Identify the cell.
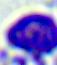

This is a leukocyte.

magnification: 400x
modality: micrograph